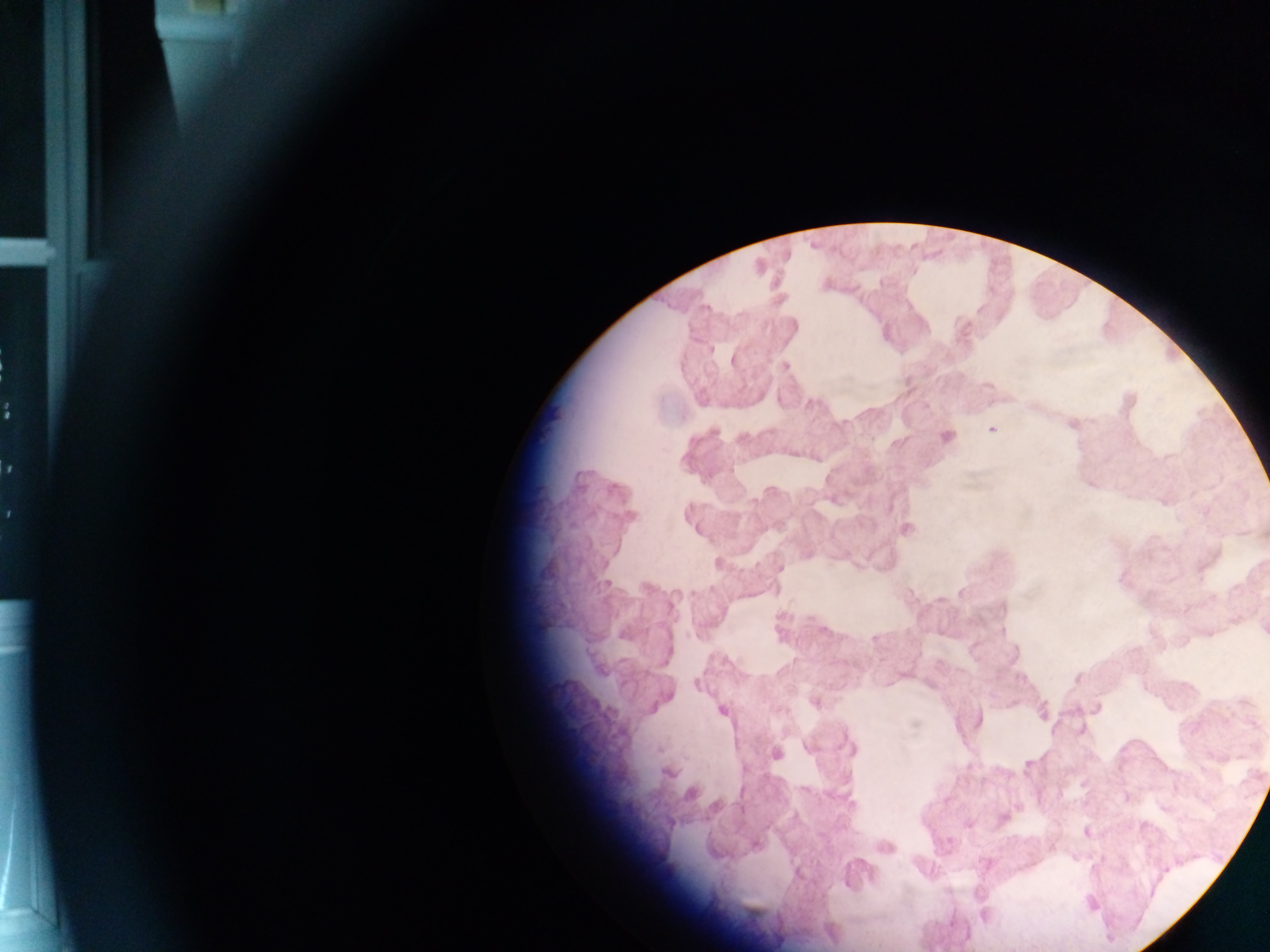

preparation = thick blood smear
capture = mobile-phone photograph through a microscope
country = Ghana
malaria parasite locations = approximate centers as x y in pixels: 979 309; 734 359; 785 366; 992 429; 946 437; 907 530; 780 568; 823 630; 815 703; 722 711; 915 724; 1253 724; 850 749; 776 754; 967 824; 1086 832; 984 915
image size = 1270×952 pixels
field of view = single